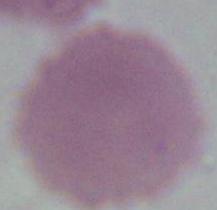
Summary:
  - Magnification: 1000x
  - Modality: micrograph
  - Identification: red blood cell